Point out each Plasmodium parasite.
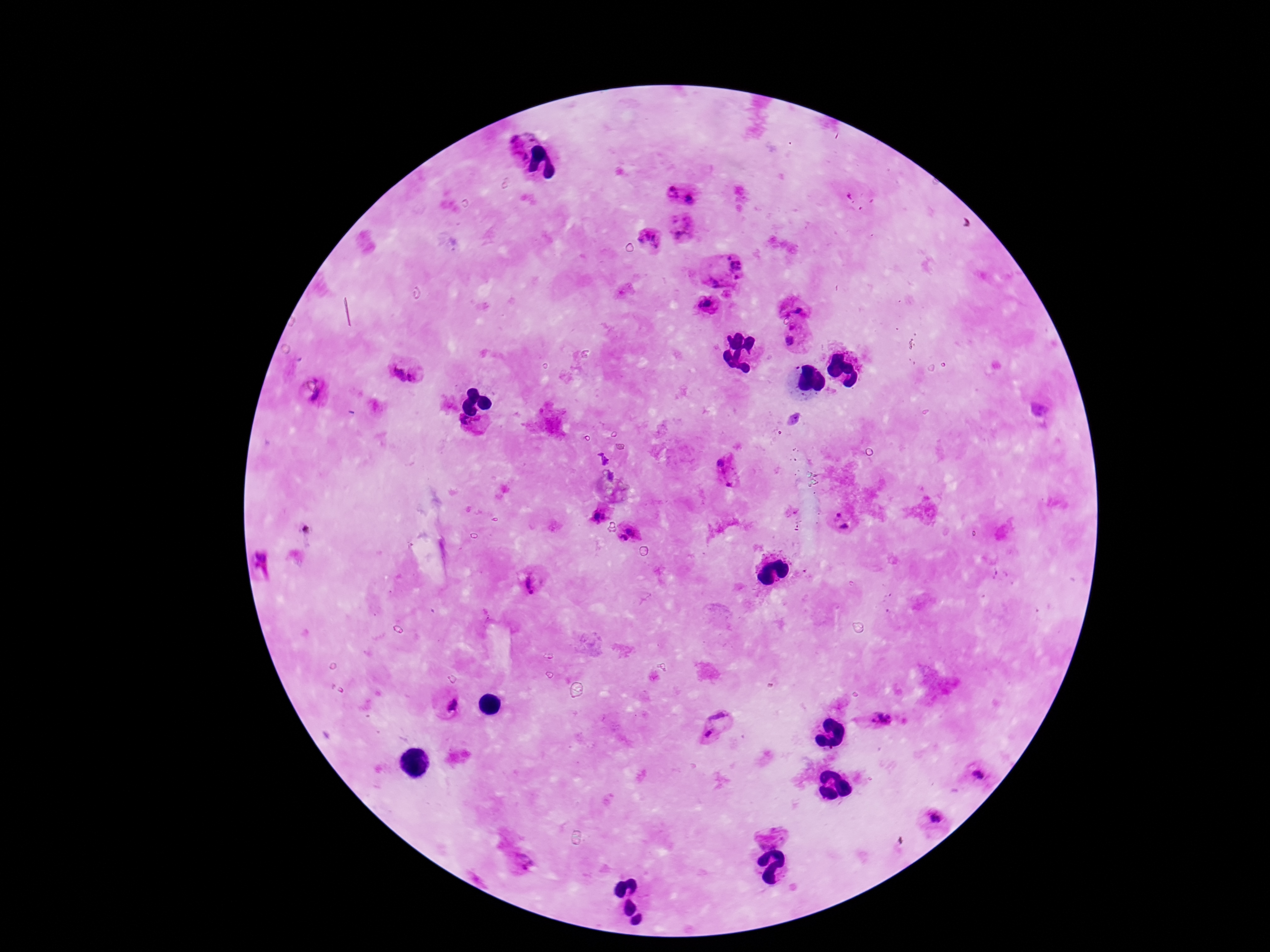
Approximate centers as {x, y} in pixels.
Plasmodium parasites: {517, 147}, {672, 194}, {693, 200}, {682, 228}, {649, 241}, {739, 264}, {714, 282}, {707, 305}, {802, 307}, {793, 338}, {399, 374}, {414, 377}, {318, 396}, {468, 426}, {724, 460}, {729, 481}, {838, 513}, {601, 515}, {845, 528}, {630, 530}, {623, 538}, {261, 556}, {532, 580}, {449, 703}, {720, 712}, {881, 719}, {711, 735}, {979, 775}, {936, 818}, {770, 835}, {522, 859}.

{
  "field_of_view": "one from this slide",
  "stain": "Giemsa",
  "preparation": "thick blood smear",
  "image_size": "1270×952 pixels",
  "capture": "smartphone camera through the microscope eyepiece",
  "patient_malaria_status": "positive",
  "magnification": "100x"
}